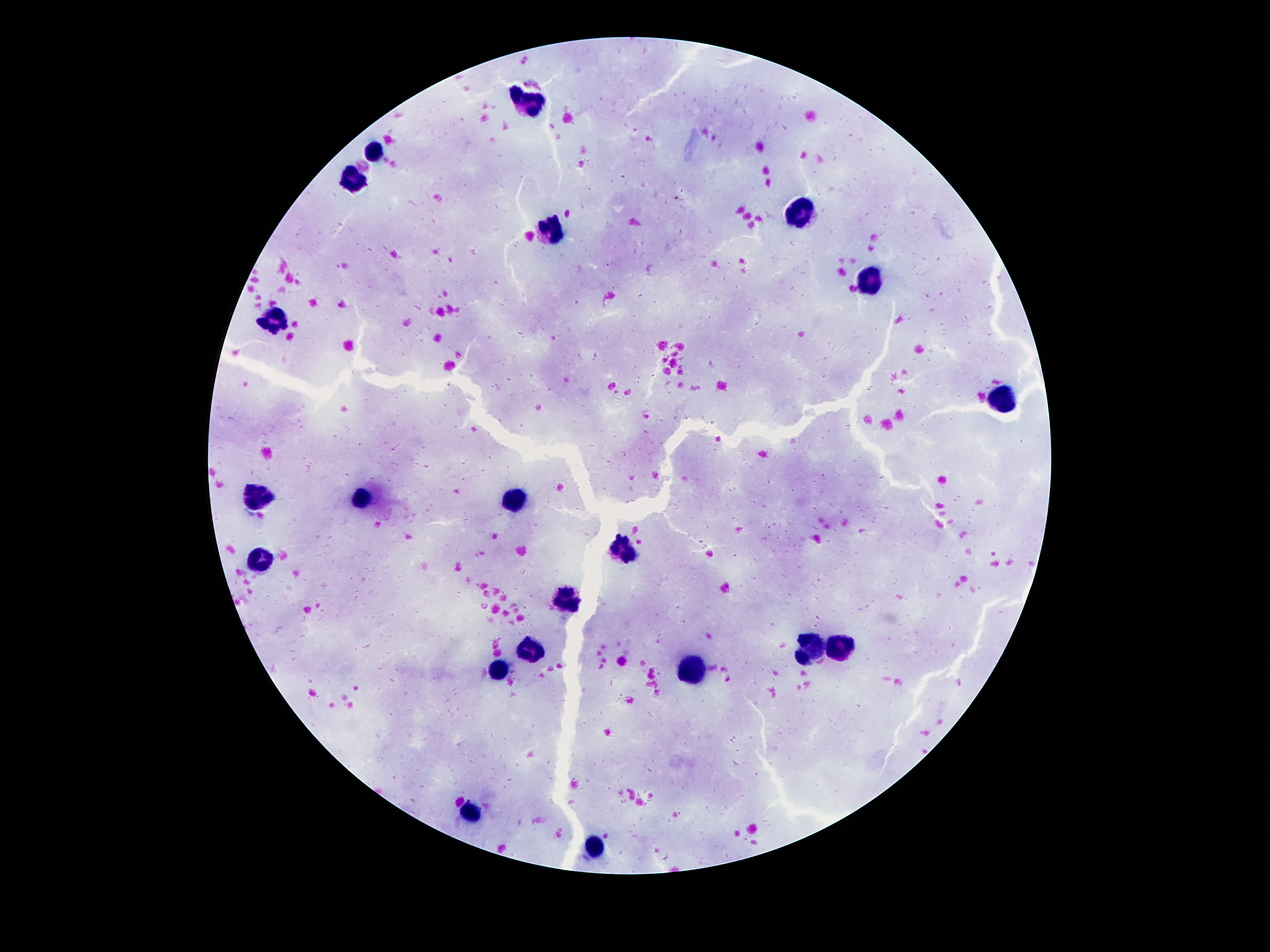

Approximate object centers, in pixels from the top-left corner.
Summary:
  - Leukocyte locations: (x=533, y=103), (x=376, y=153), (x=352, y=181), (x=802, y=218), (x=552, y=233), (x=871, y=282), (x=274, y=321), (x=1005, y=396), (x=512, y=495), (x=361, y=498), (x=255, y=499), (x=626, y=551), (x=259, y=560), (x=563, y=600), (x=839, y=648), (x=809, y=651), (x=529, y=654), (x=695, y=672), (x=499, y=674), (x=471, y=811), (x=593, y=846)
  - Stain: Giemsa
  - Image size: 1270×952 pixels
  - Field of view: one from this slide
  - Preparation: thick blood film
  - Patient malaria status: not infected
  - Capture: smartphone camera through the microscope eyepiece
  - Magnification: 100x